Point out every malaria parasite.
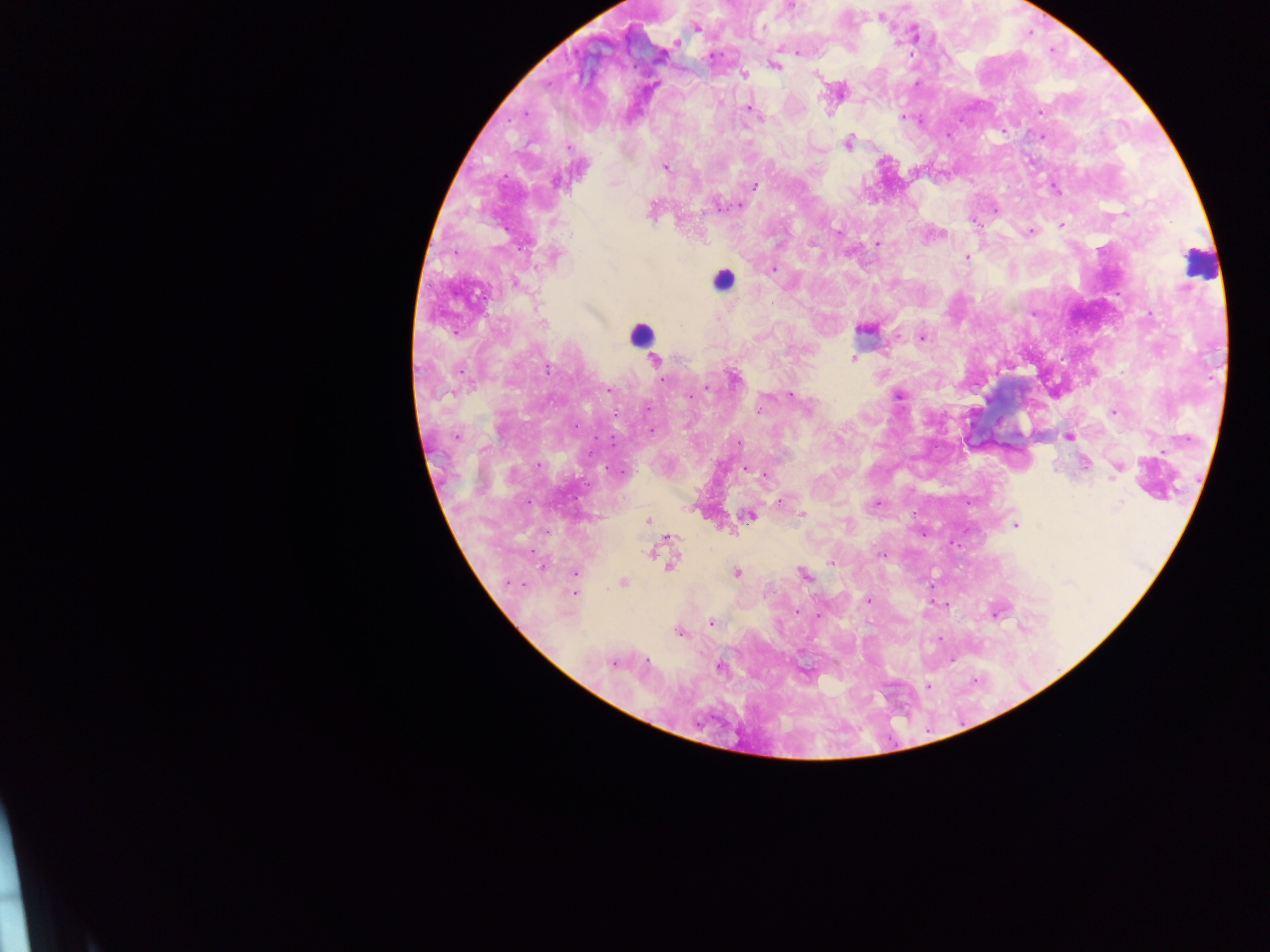

Approximate centers as [x, y] in pixels.
Malaria parasites: [792, 6], [787, 9], [880, 17], [695, 26], [762, 26], [915, 32], [917, 37], [796, 52], [777, 65], [743, 74], [815, 76], [827, 103], [749, 109], [1041, 112], [525, 114], [903, 115], [760, 118], [847, 143], [566, 147], [664, 167], [555, 181], [614, 184], [755, 185], [1056, 189], [717, 203], [740, 204], [650, 214], [971, 219], [1061, 225], [838, 230], [1030, 232], [940, 233], [813, 244], [878, 244], [966, 257], [771, 269], [864, 329], [924, 337], [852, 359], [654, 361], [547, 367], [735, 378], [664, 379], [707, 387], [608, 391], [789, 395], [900, 395], [688, 398], [758, 406], [1115, 411], [576, 425], [651, 431], [457, 436], [1069, 438], [739, 445], [1140, 461], [1086, 462], [1119, 464], [745, 471], [764, 475], [1114, 478], [781, 502], [875, 502], [1119, 507], [695, 509], [802, 514], [750, 518], [646, 519], [1016, 526], [731, 529], [664, 539], [649, 553], [880, 554], [670, 560], [830, 562], [545, 568], [574, 572], [737, 573], [804, 577], [623, 582], [575, 593], [867, 599], [941, 605], [945, 606], [999, 612], [994, 614], [822, 615], [710, 623], [1022, 627], [678, 632], [613, 662], [718, 666], [927, 686].

image_size: 1270×952 pixels
field_of_view: single
preparation: thick blood smear
leukocyte_locations: 'approximate centers as [x, y] in pixels: [1196, 273], [723, 284], [641, 331]'
capture: mobile-phone photograph through a microscope
country: Ghana